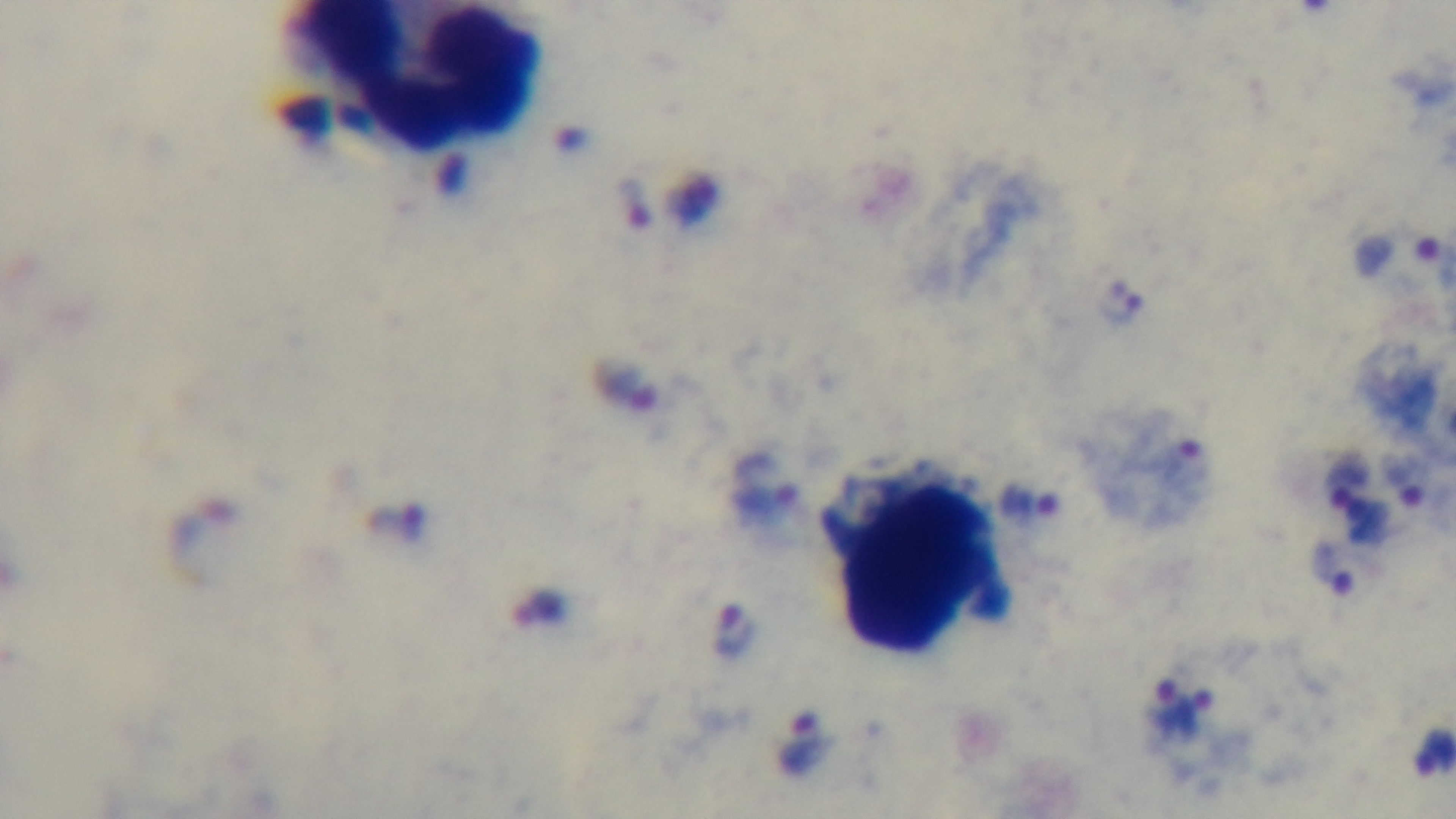

Preparation: thick. One field from the slide. Giemsa stain. 100x oil-immersion objective. Light microscopy. Captured with a mounted 4K digital camera. Malaria status: positive.